Classify this cell by malaria status.
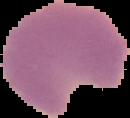
It is parasitized.

From a thin blood film. Image is 130×118 pixels. Cell region segmented out of the field of view; the surrounding area is masked to black.